Give the position of each P. falciparum parasite with its life-cycle stage, each leukocyte, and any debris.
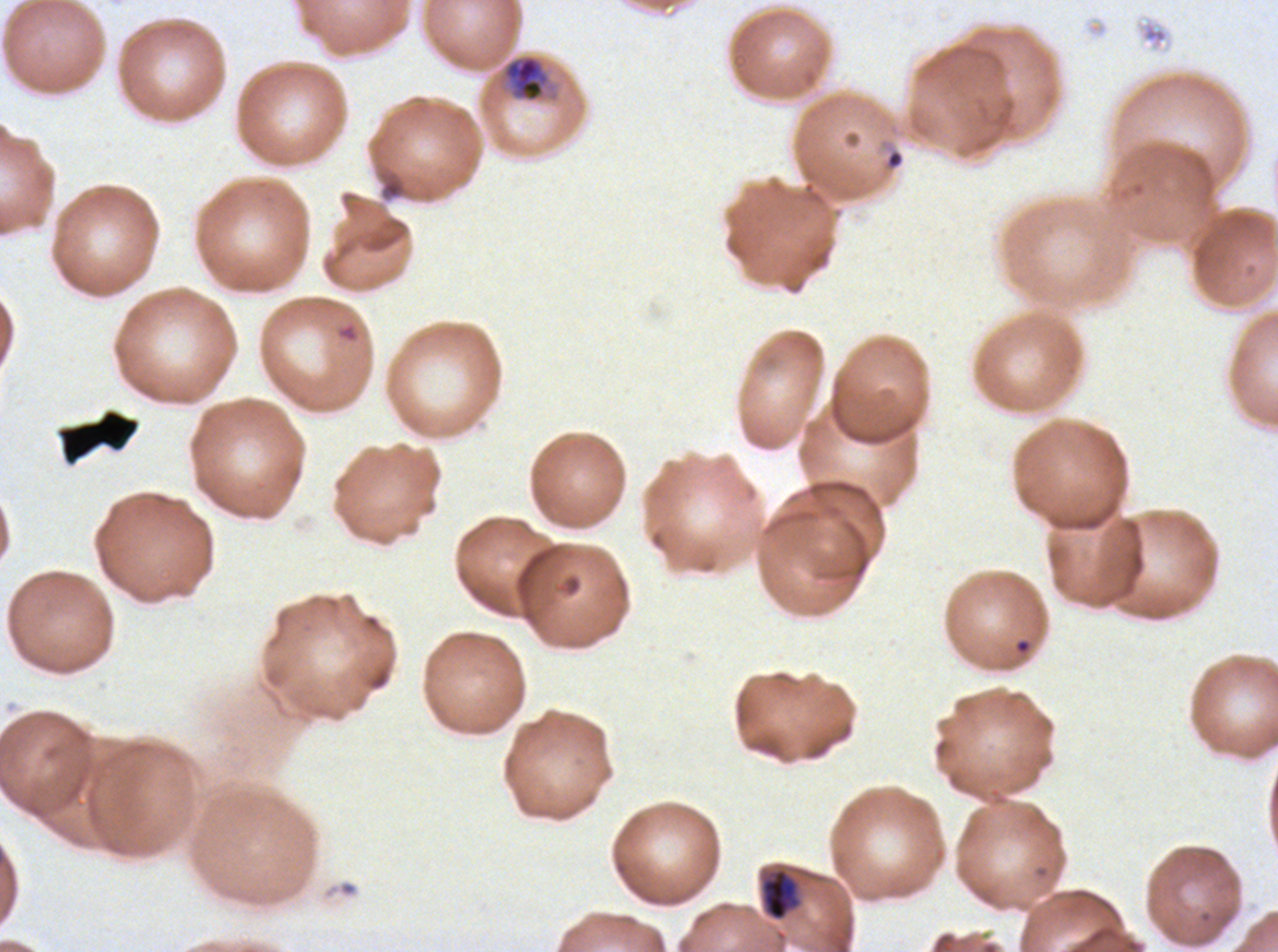

Approximate bounding rectangles given as corner coordinates in pixels from the top-left.
Rings: (x1=883, y1=147, x2=905, y2=172).
Late-ring/early-trophozoite forms: (x1=761, y1=869, x2=796, y2=921).
Mid trophozoites: (x1=498, y1=53, x2=559, y2=104).
Debris: (x1=58, y1=409, x2=140, y2=464).
No late trophozoites, early schizonts, late schizonts, segmenters, gametocytes, or leukocytes observed.

preparation = thin blood smear
stain = Giemsa
image size = 1278×952 pixels
field of view = sub-image separated from a larger composite
specimen = P. falciparum from a patient in The Gambia, cultured ex vivo for 24 to 48 hours
life-cycle stages observed = ring, late-ring/early-trophozoite, mid trophozoite